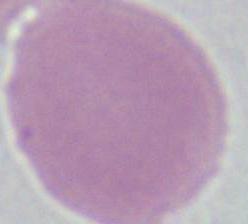
An erythrocyte is seen. Micrograph. 1000x magnification.